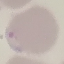

Summary:
  - Result: malaria parasites identified
  - Capture: smartphone camera at the microscope eyepiece
  - Preparation: thin blood smear
  - Stain: Giemsa
  - Image type: automatically extracted cell patch, resized to 64 × 64 pixels